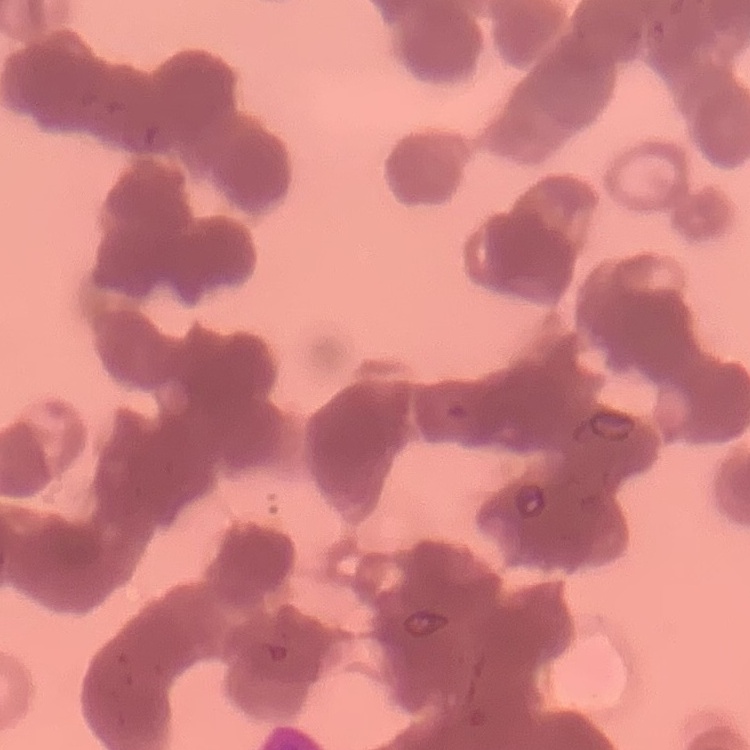

Summary:
  - Red blood cell morphology: rouleaux formation
  - Image type: square crop of a larger photomicrograph
  - Preparation: thin blood smear
  - Stain: Field's or Giemsa